Identify the cell.
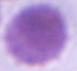

This is an erythrocyte.

Summary:
  - Modality: photomicrograph
  - Magnification: 1000x